Report the malaria status of this cell.
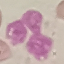

Uninfected.

{
  "stain": "Giemsa",
  "preparation": "thin blood smear",
  "capture": "smartphone camera at the microscope eyepiece",
  "image_type": "automatically extracted cell patch, resized to 64 × 64 pixels"
}